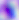
modality = micrograph
identification = Toxoplasma gondii
magnification = 400x